State the preparation type.
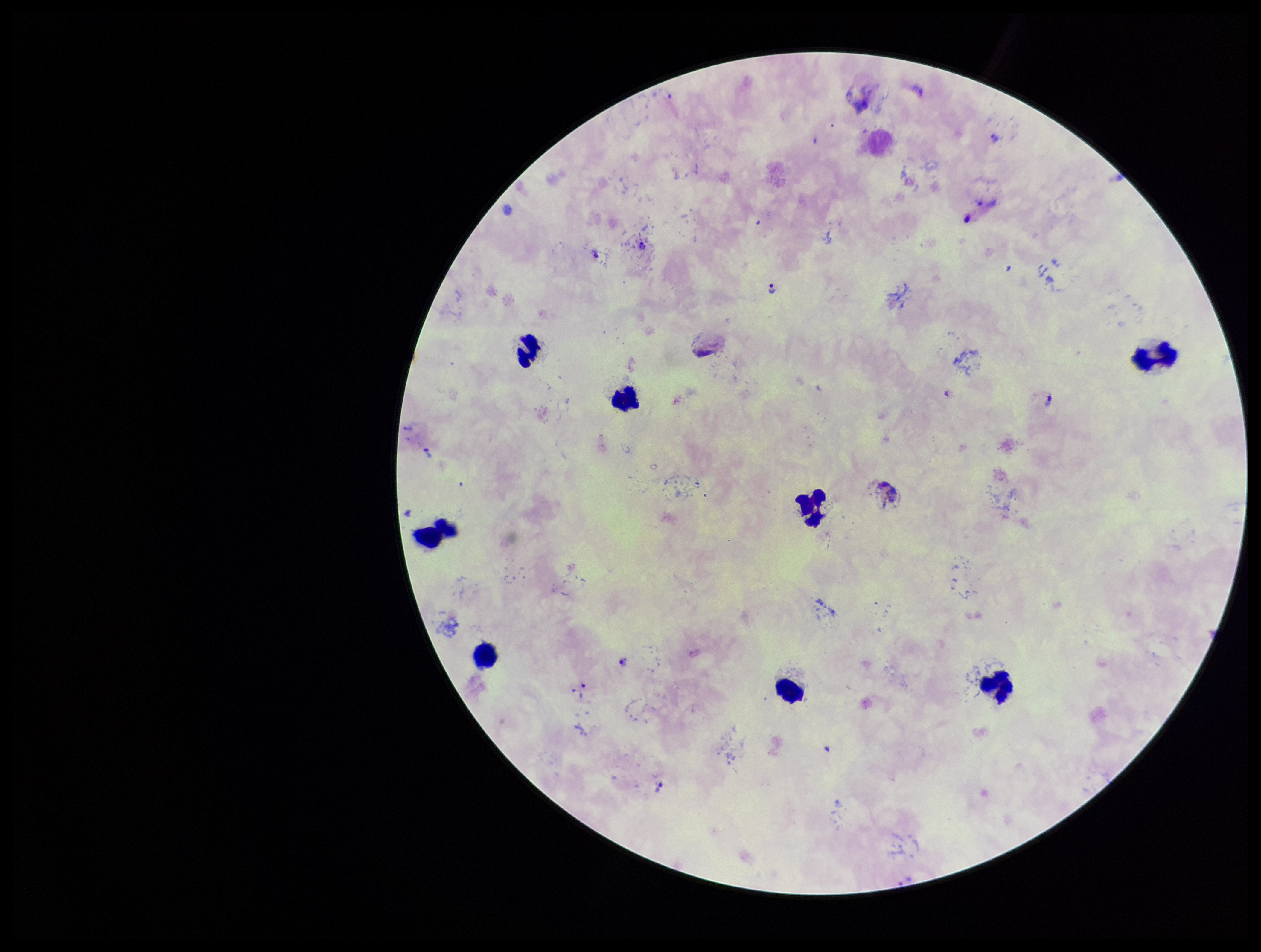
It is a thick blood smear.

One field from this slide. Leukocyte count: 9. Parasite count: 11. Patient malaria status: positive. Giemsa stain. Smartphone photograph taken through the eyepiece of a microscope. Image is 1261×952 pixels. Species reported for this patient: Plasmodium vivax. Plasmodium parasites: seen.